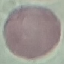

Malaria status: uninfected. Thin smear of blood. Acquired by smartphone through the microscope eyepiece. Automatically extracted cell patch, resized to 64 × 64 pixels. Giemsa stain.